Identify the parasite.
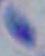
This is Toxoplasma gondii.

1000x magnification. Micrograph.